Give the extent of all Plasmodium falciparum-infected red blood cells.
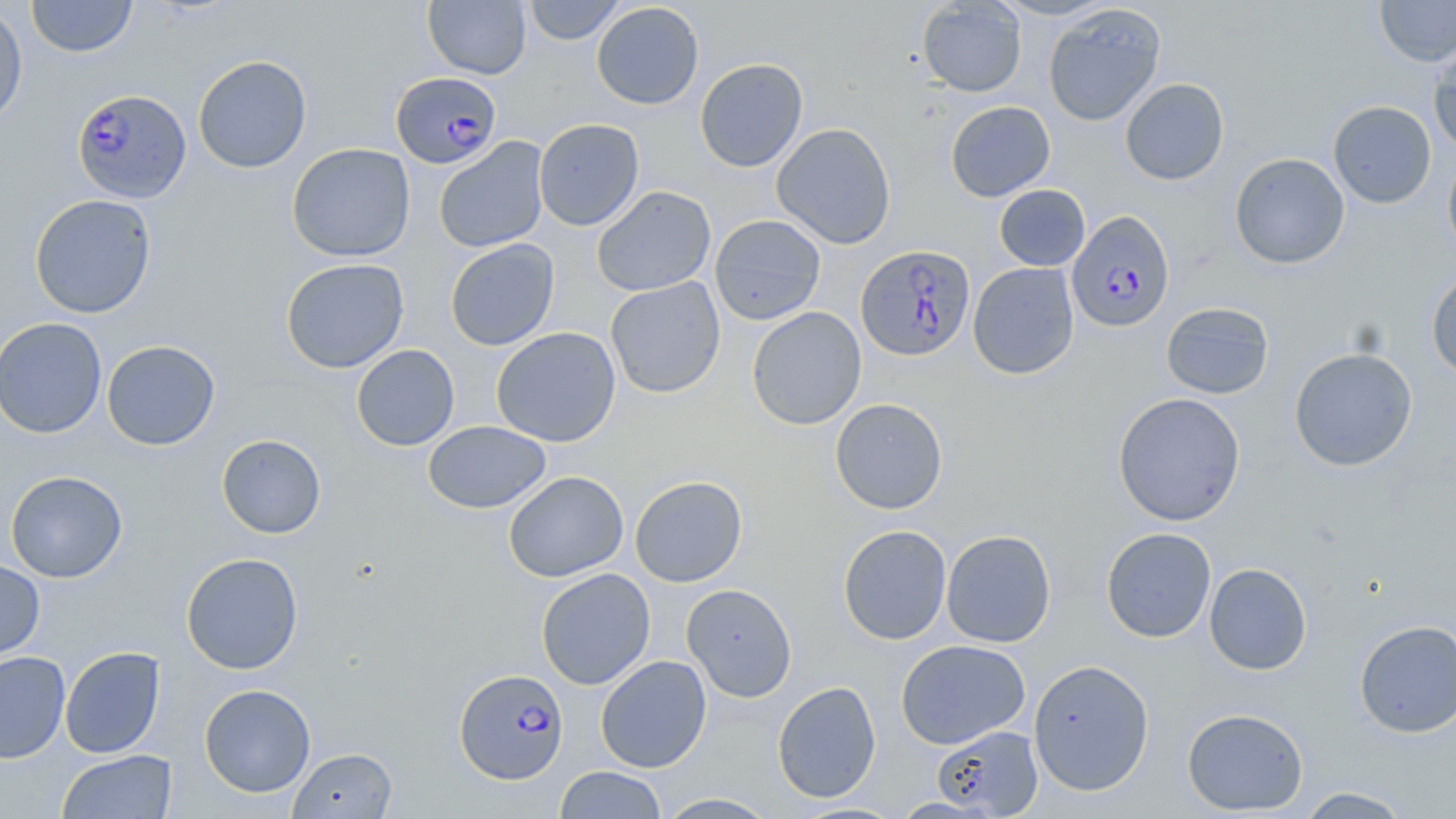
Approximate bounding boxes as (x1, y1, x2, y2) in pixels.
Plasmodium falciparum-infected red blood cells: (390, 71, 502, 169), (72, 89, 191, 203), (1067, 210, 1174, 331), (856, 244, 976, 361), (455, 668, 568, 784).

Uninfected red blood cell locations: (26, 0, 138, 58), (523, 0, 627, 44), (990, 0, 1118, 20), (1374, 0, 1456, 67), (423, 1, 531, 79), (917, 1, 1027, 97), (591, 2, 704, 110), (0, 3, 28, 129), (1043, 5, 1166, 126), (1428, 39, 1456, 156), (192, 55, 312, 174), (694, 58, 808, 172), (1120, 78, 1230, 185), (1328, 100, 1437, 209), (945, 101, 1055, 202), (533, 118, 645, 231), (771, 122, 896, 249), (433, 137, 550, 253), (287, 143, 415, 262), (1443, 149, 1456, 264), (1229, 153, 1350, 270), (994, 184, 1090, 271), (591, 185, 716, 297), (29, 194, 157, 319), (709, 214, 826, 325), (445, 238, 559, 351), (280, 258, 410, 374), (968, 262, 1079, 379), (1426, 267, 1456, 381), (605, 277, 725, 398), (1161, 302, 1274, 399), (747, 307, 867, 430), (0, 317, 107, 439), (491, 327, 621, 447), (101, 340, 221, 450), (351, 344, 460, 451), (1289, 347, 1418, 471), (1113, 392, 1246, 526), (830, 398, 948, 514), (423, 420, 551, 514), (216, 434, 326, 539), (5, 470, 128, 583), (503, 470, 628, 582), (630, 475, 747, 587), (838, 524, 952, 644), (1101, 526, 1216, 642), (941, 529, 1056, 647), (180, 552, 304, 674), (0, 558, 45, 663), (1204, 562, 1313, 675), (536, 568, 656, 689), (681, 584, 797, 702), (1354, 620, 1456, 737), (895, 639, 1030, 749), (59, 646, 166, 758), (0, 651, 71, 763), (595, 655, 712, 772), (1028, 659, 1155, 796), (772, 681, 882, 804), (199, 683, 316, 797), (1182, 707, 1309, 815), (931, 725, 1043, 817), (288, 746, 398, 818), (57, 750, 177, 818), (554, 766, 668, 818), (1295, 786, 1414, 818), (655, 792, 780, 818), (889, 797, 1002, 818), (790, 801, 906, 818). Slide-level diagnosis: Plasmodium falciparum. Captured at 1000x magnification. Image is 1456×819 pixels. Single field of view. Thin blood smear. May-Grünwald-Giemsa stain. Light microscopy.